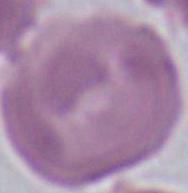 An erythrocyte is shown. Captured at 1000x magnification. Photomicrograph.